Assess this cell for malaria.
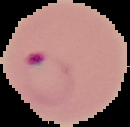

It is parasitized.

Summary:
  - Image size: 130×127 pixels
  - Preparation: thin blood film
  - Image type: segmented cell region on a black background